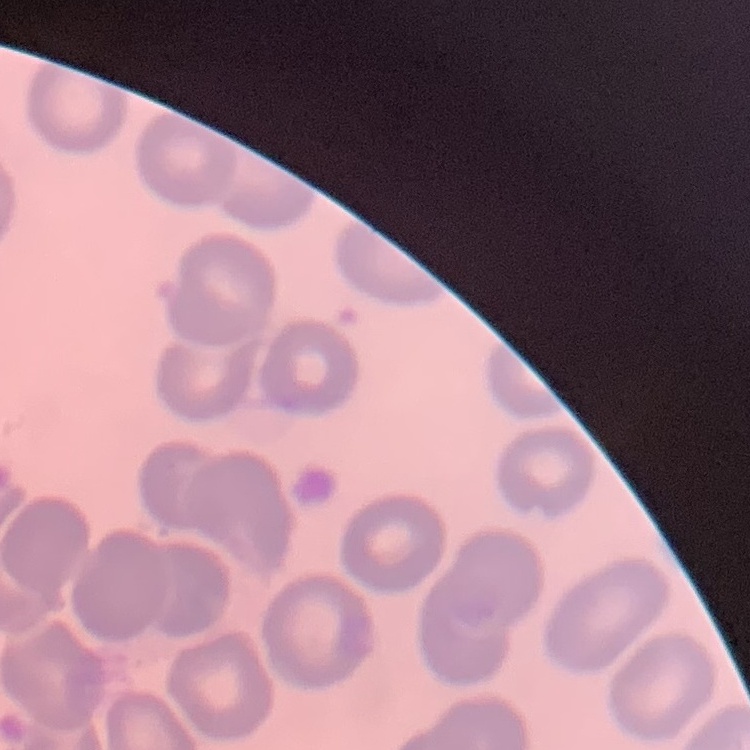

The erythrocytes exhibit no rouleaux formation. Thin blood smear. One tile cut from a larger photomicrograph. Field's or Giemsa stain.